State which parasite is depicted.
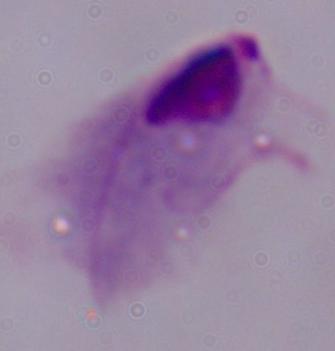

A trichomonad.

modality = micrograph
magnification = 1000x